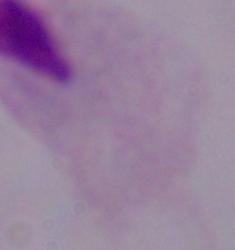

Captured at 1000x magnification. A trichomonad is seen. Photomicrograph.